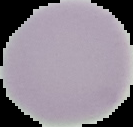 Segmented cell region on a black background. From a thin blood film. Image is 133×127 pixels. Malaria status: uninfected.